Report the malaria status of this cell.
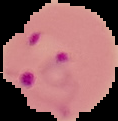
It is parasitized.

image size = 118×121 pixels
preparation = thin blood film
image type = segmented cell region with the area outside set to black